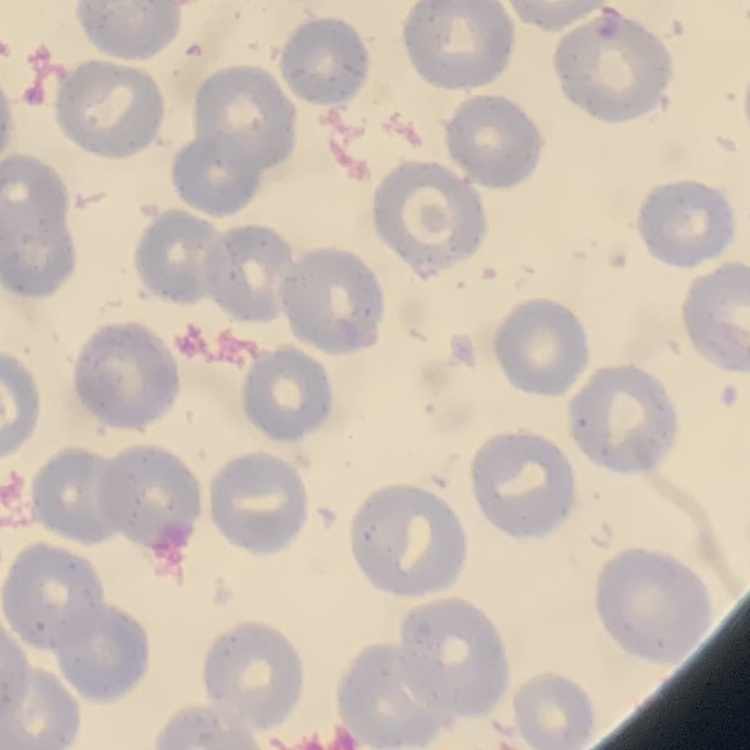

erythrocyte_morphology: no rouleaux formation
stain: Field's or Giemsa
preparation: thin blood smear
image_type: square crop of a larger photomicrograph